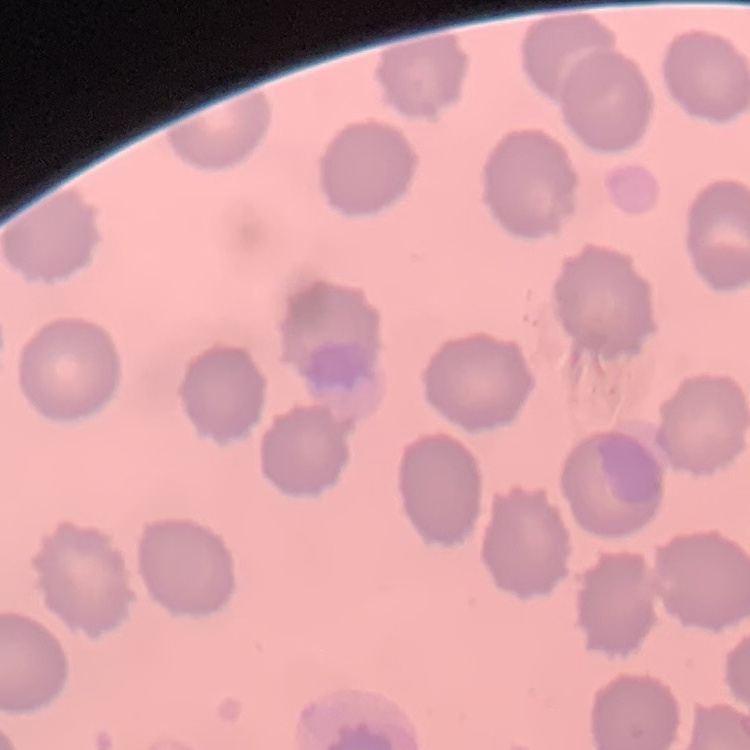
The red blood cells exhibit no rouleaux formation. Stained with either Field's or Giemsa. One tile cut from a larger photomicrograph. Thin peripheral smear.